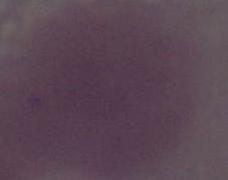
Photomicrograph. A red blood cell is shown. Captured at 1000x magnification.